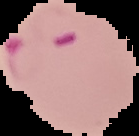

image size = 139×136 pixels
result = malaria parasites identified
image type = segmented cell region with the area outside set to black
preparation = thin blood film